Classify this cell by malaria status.
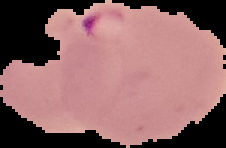
Parasitized.

image type = segmented cell region with the area outside set to black
image size = 226×148 pixels
preparation = thin blood film